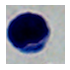
modality = micrograph
identification = leukocyte
magnification = 1000x